Report the malaria status of this cell.
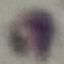

It is uninfected.

Giemsa stain. Automatically extracted cell patch, resized to 64 × 64 pixels. Acquired by smartphone through the microscope eyepiece. Thin blood smear.